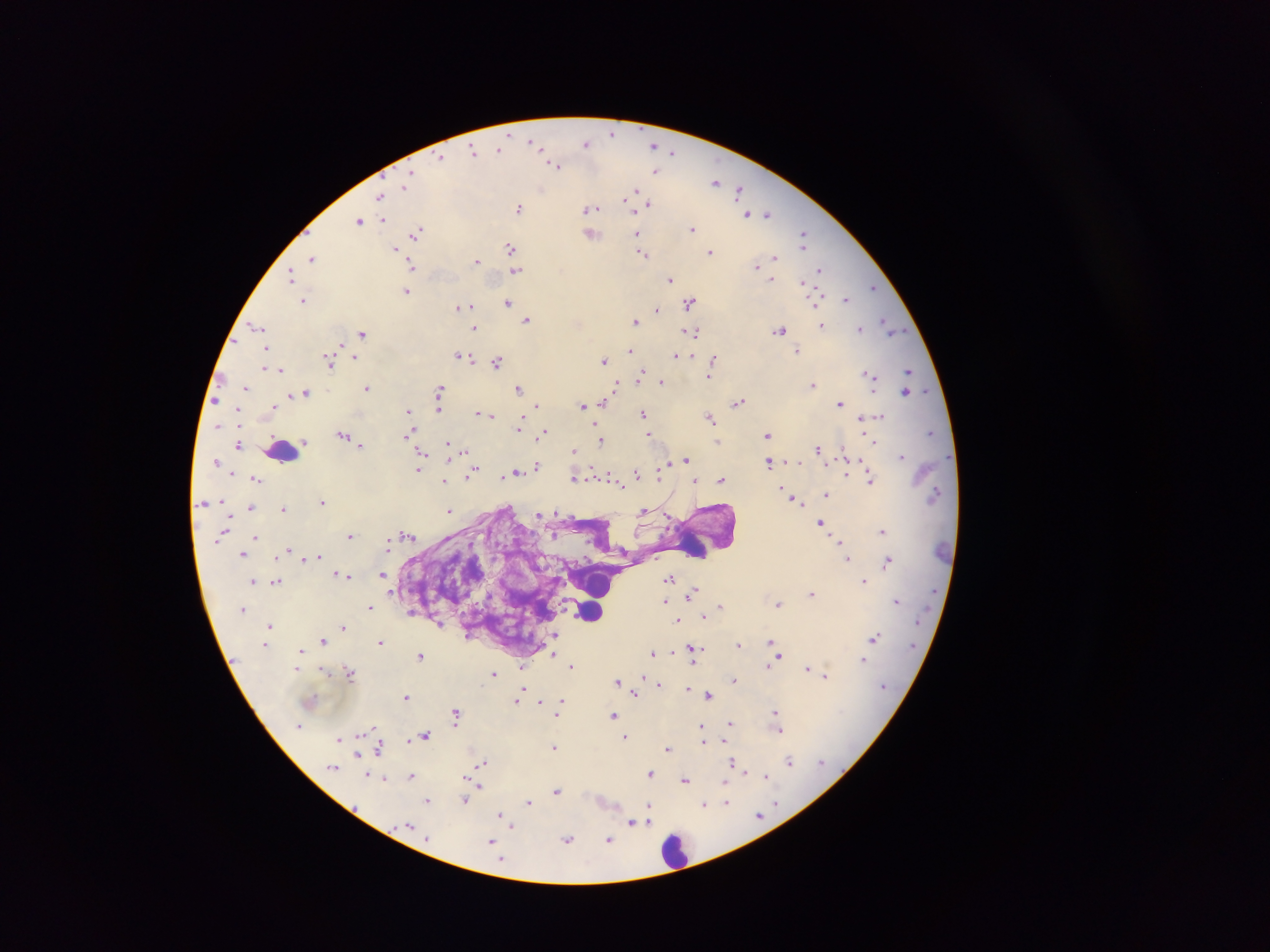
Approximate centers as [x, y] in pixels.
Summary:
  - Plasmodium parasite locations: [612, 133], [532, 142], [586, 143], [653, 145], [499, 148], [473, 152], [673, 152], [441, 157], [554, 165], [655, 170], [407, 180], [715, 181], [404, 186], [541, 188], [635, 190], [738, 190], [380, 196], [650, 204], [519, 208], [589, 208], [746, 214], [767, 214], [359, 220], [383, 220], [692, 228], [417, 231], [637, 234], [591, 235], [803, 237], [510, 247], [395, 248], [711, 252], [642, 254], [313, 257], [775, 257], [476, 261], [412, 266], [756, 266], [515, 270], [820, 270], [291, 276], [670, 280], [805, 286], [872, 287], [407, 291], [302, 300], [846, 300], [690, 302], [507, 303], [459, 307], [658, 309], [526, 319], [635, 320], [884, 321], [822, 325], [257, 326], [889, 326], [475, 328], [858, 328], [779, 330], [694, 331], [894, 331], [363, 333], [340, 345], [265, 348], [631, 350], [797, 352], [462, 356], [677, 356], [355, 357], [714, 360], [603, 361], [329, 362], [498, 362], [265, 369], [281, 370], [907, 371], [709, 375], [870, 375], [640, 377], [660, 382], [812, 384], [616, 386], [246, 387], [367, 387], [519, 388], [439, 390], [905, 392], [306, 393], [291, 395], [604, 402], [738, 402], [840, 404], [537, 405], [438, 406], [581, 406], [408, 412], [481, 414], [643, 414], [491, 415], [710, 417], [860, 417], [879, 417], [409, 418], [519, 428], [409, 432], [544, 432], [930, 433], [649, 435], [768, 435], [343, 436], [601, 440], [303, 441], [875, 442], [448, 444], [239, 445], [360, 445], [818, 449], [574, 451], [464, 452], [901, 456], [421, 458], [685, 459], [769, 462], [537, 465], [663, 468], [418, 470], [474, 472], [516, 473], [636, 473], [847, 474], [659, 475], [502, 477], [610, 477], [573, 478], [256, 479], [721, 479], [871, 479], [444, 481], [695, 481], [619, 482], [781, 489], [827, 494], [795, 500], [220, 501], [205, 502], [322, 502], [251, 507], [283, 509], [450, 511], [644, 511], [555, 512], [539, 515], [820, 522], [883, 531], [408, 535], [255, 536], [350, 536], [840, 541], [288, 550], [243, 554], [318, 556], [848, 559], [888, 561], [341, 575], [383, 575], [347, 576], [669, 578], [864, 580], [252, 581], [276, 581], [692, 593], [811, 594], [664, 600], [896, 601], [778, 604], [721, 605], [370, 606], [705, 618], [677, 621], [270, 625], [343, 627], [554, 634], [874, 637], [324, 641], [771, 641], [381, 642], [738, 644], [694, 648], [301, 650], [652, 652], [673, 652], [553, 654], [420, 655], [778, 657], [863, 659], [769, 664], [571, 666], [522, 668], [808, 668], [297, 669], [321, 670], [348, 672], [493, 674], [825, 676], [645, 679], [734, 680], [618, 681], [658, 684], [687, 689], [521, 693], [635, 693], [709, 695], [406, 697], [518, 698], [541, 701], [561, 702], [558, 711], [775, 711], [456, 714], [613, 715], [730, 724], [702, 728], [780, 730], [424, 736], [625, 737], [340, 738], [703, 741], [554, 747], [381, 748], [667, 749], [358, 755], [789, 761], [482, 762], [734, 762], [333, 767], [650, 774], [376, 776], [411, 776], [766, 776], [383, 779], [684, 780], [725, 784], [478, 786], [557, 791], [465, 800], [428, 801], [529, 802], [726, 803], [705, 804], [649, 805], [759, 815], [503, 817], [648, 817], [632, 822], [511, 826], [567, 839], [609, 840], [491, 843]
  - Leukocyte locations: [280, 453], [695, 544], [601, 586], [590, 611], [676, 852]
  - Country: Ghana
  - Capture: mobile-phone photograph through a microscope
  - Preparation: thick blood film
  - Field of view: single
  - Image size: 1270×952 pixels